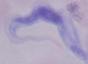 A trypanosome is seen. Captured at 1000x magnification. Micrograph.